Assess the morphology of the red blood cells.
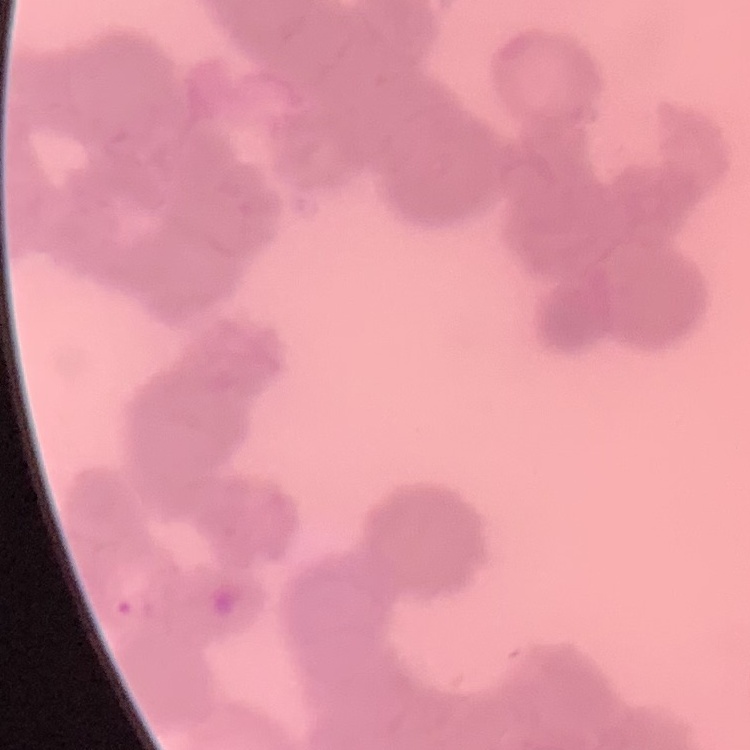

They show rouleaux formation.

Thin peripheral smear. Stained with either Field's or Giemsa. Square crop of a larger photomicrograph.